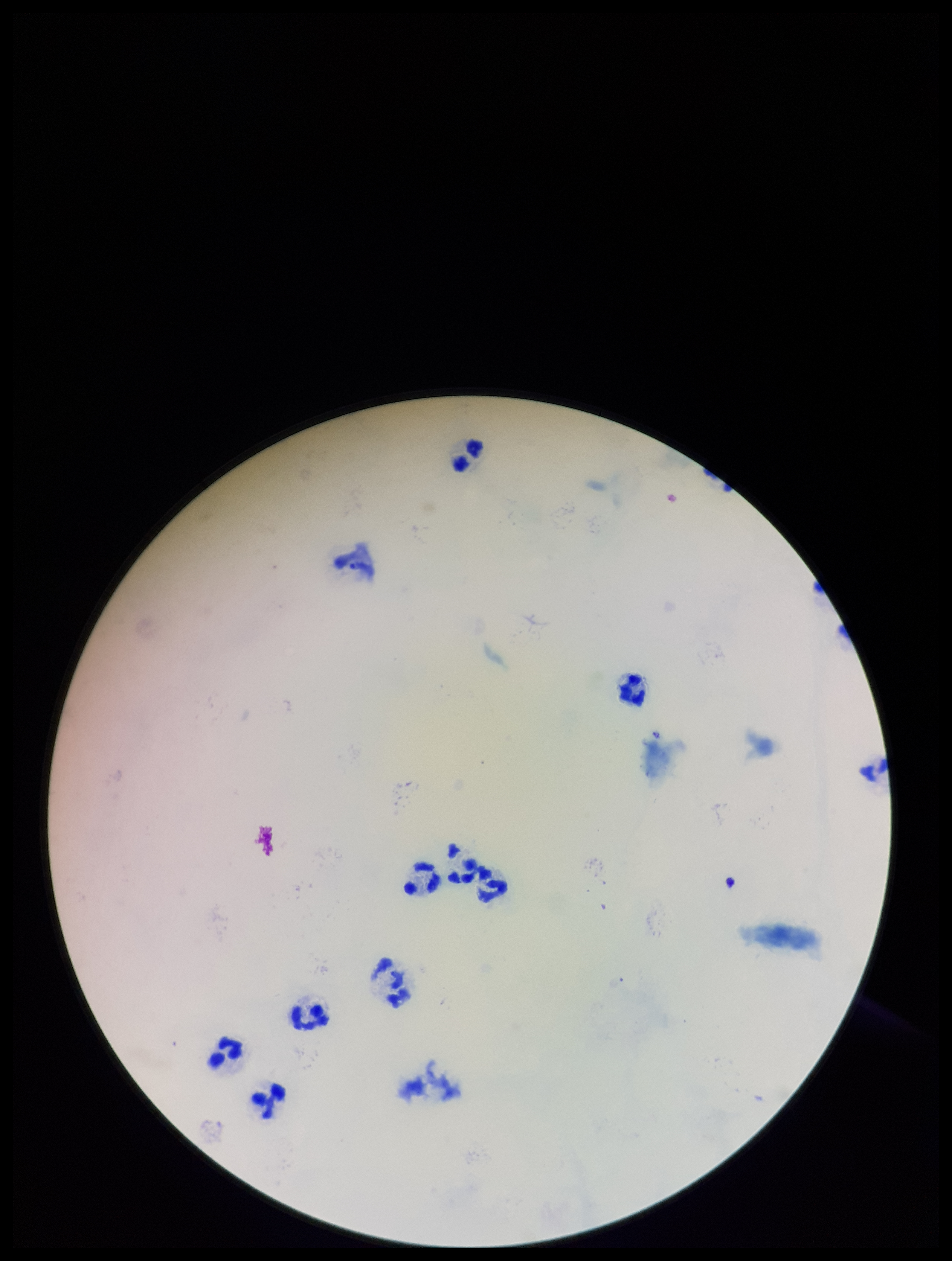
preparation: thick smear
stain: Giemsa
capture: smartphone photograph through the microscope eyepiece
parasite_count: 0
image_size: 952×1261 pixels
plasmodium_parasites: none detected
patient_malaria_status: negative
leukocyte_count: 9
field_of_view: one from this slide